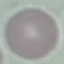
Summary:
  - Result: negative for malaria parasites
  - Preparation: thin smear
  - Image type: automatically extracted cell patch, resized to 64 × 64 pixels
  - Stain: Giemsa
  - Capture: smartphone camera at the microscope eyepiece